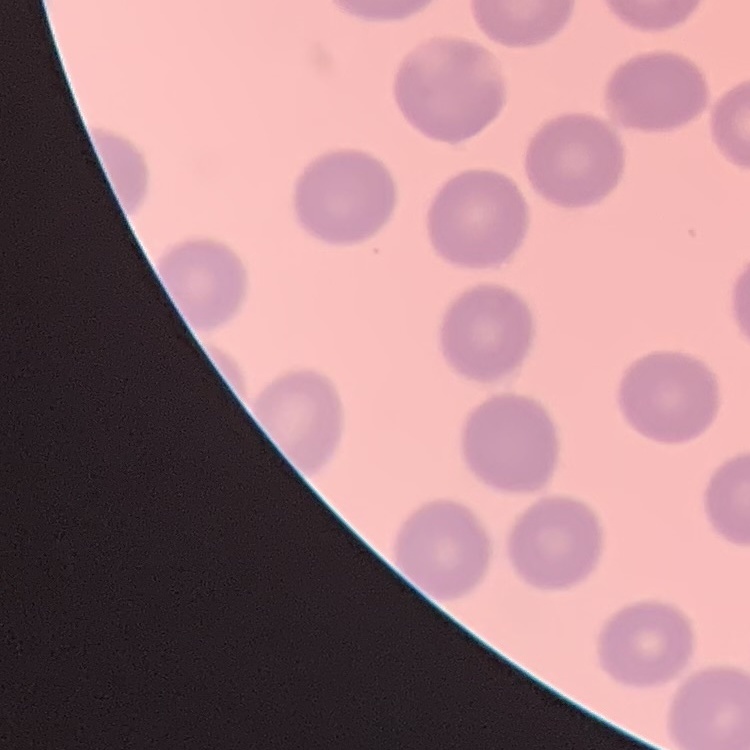
Summary:
  - Red blood cell morphology: no rouleaux formation
  - Preparation: thin blood smear
  - Image type: square crop of a larger photomicrograph
  - Stain: Field's or Giemsa